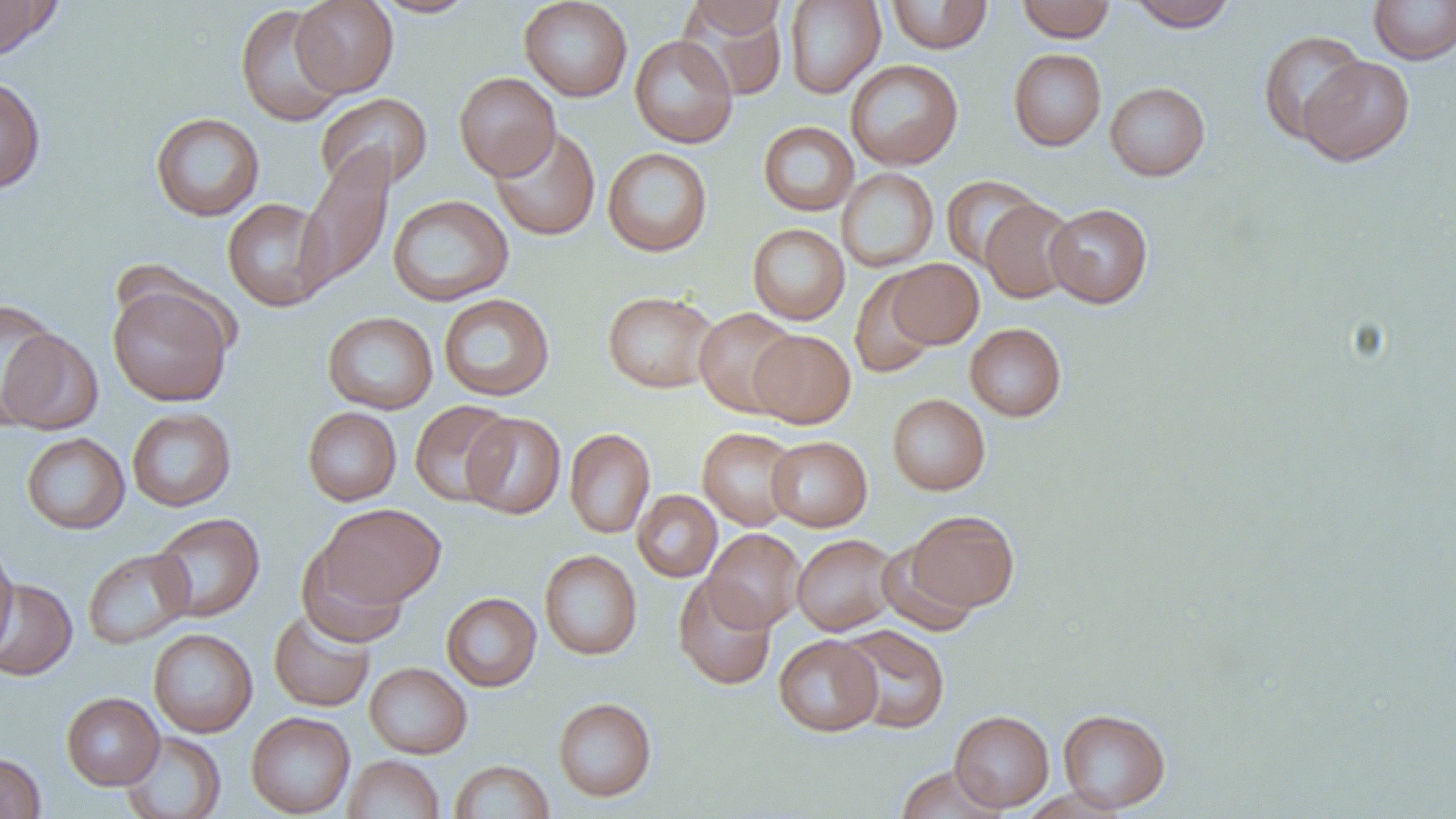

Summary:
  - Coordinate format: approximate bounding boxes as (x1,y1)-(x2,y2) corner pairs in pixels
  - Uninfected red blood cell locations: (0,0)-(60,60), (291,0)-(399,97), (370,0)-(481,17), (519,0)-(633,102), (687,0)-(787,40), (885,0)-(993,54), (1016,0)-(1115,42), (1125,0)-(1238,31), (1368,0)-(1456,65), (784,1)-(885,99), (234,4)-(347,127), (683,5)-(788,100), (1257,29)-(1368,144), (629,35)-(738,148), (1008,48)-(1106,151), (1299,57)-(1414,166), (845,59)-(963,170), (454,72)-(561,180), (0,74)-(46,194), (1105,81)-(1210,181), (314,92)-(433,193), (150,112)-(265,221), (758,121)-(859,216), (489,125)-(601,240), (295,145)-(395,295), (603,147)-(713,257), (837,168)-(938,272), (941,175)-(1043,269), (387,194)-(514,306), (222,198)-(332,312), (980,198)-(1078,303), (1044,203)-(1153,308), (748,223)-(849,325), (887,258)-(984,349), (849,270)-(938,378), (107,281)-(234,407), (602,291)-(719,393), (438,293)-(555,401), (694,307)-(801,418), (322,311)-(438,414), (965,323)-(1066,421), (1,324)-(103,436), (749,329)-(855,428), (887,394)-(990,495), (409,400)-(515,506), (126,407)-(236,512), (302,407)-(401,506), (462,412)-(566,519), (697,427)-(800,531), (564,428)-(655,538), (21,433)-(129,534), (766,435)-(873,531), (632,490)-(722,582), (319,503)-(446,607), (906,510)-(1020,613), (150,513)-(264,622), (702,528)-(805,632), (791,533)-(900,636), (877,539)-(979,636), (0,540)-(18,655), (296,542)-(409,648), (82,548)-(194,649), (539,549)-(642,660), (673,575)-(776,690), (0,578)-(77,681), (441,592)-(541,691), (269,609)-(375,712), (837,624)-(949,735), (148,628)-(258,738), (774,635)-(882,736), (364,662)-(472,758), (61,692)-(164,790), (553,697)-(657,802), (1057,708)-(1170,812), (950,710)-(1054,812), (246,712)-(355,817), (120,731)-(226,818), (0,752)-(46,819), (343,754)-(444,818), (449,760)-(554,818), (894,765)-(1010,819)
  - Slide-level diagnosis: negative for blood parasites
  - Field of view: one of a larger specimen
  - Magnification: 1000x
  - Modality: light microscopy
  - Image size: 1456×819 pixels
  - Preparation: thin blood film